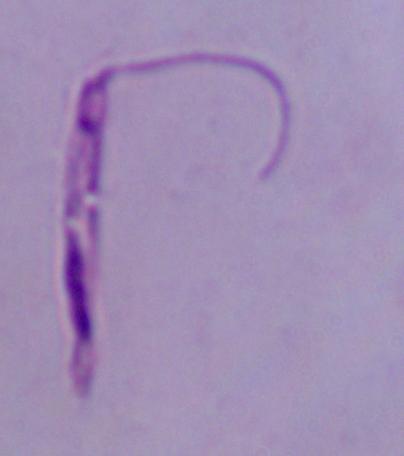
Summary:
  - Magnification: 1000x
  - Modality: micrograph
  - Identification: Leishmania